Assess the morphology of the red blood cells.
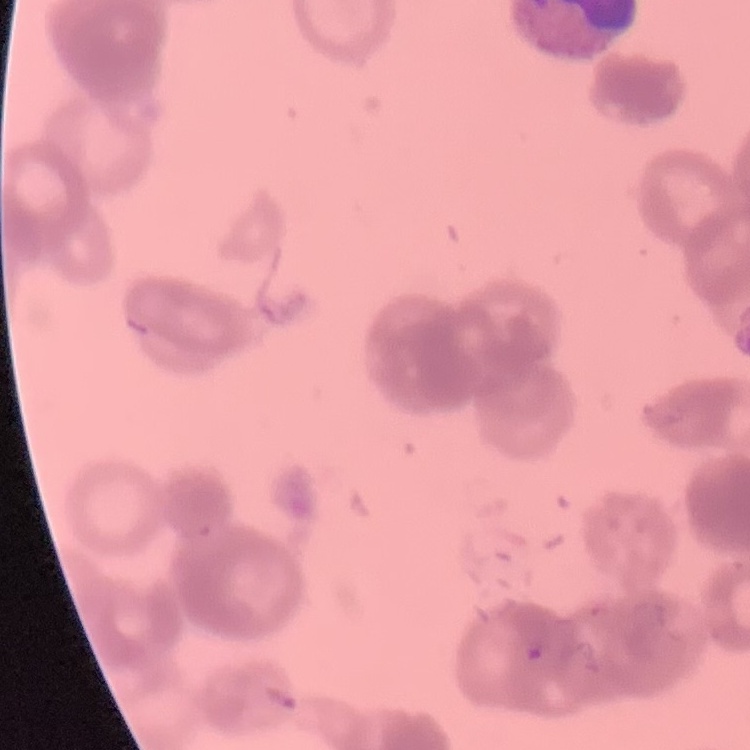
Rouleaux formation.

stain = Field's or Giemsa
preparation = thin blood film
image type = one tile cut from a larger photomicrograph